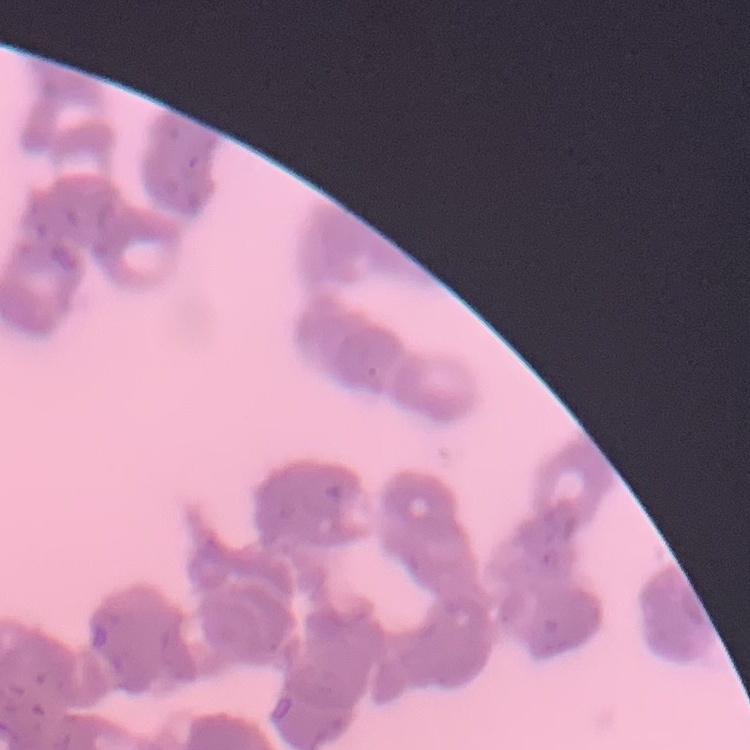
The red blood cells show rouleaux formation. Thin blood smear. Stained with either Field's or Giemsa. Square crop of a larger photomicrograph.